Give the position of every malaria parasite.
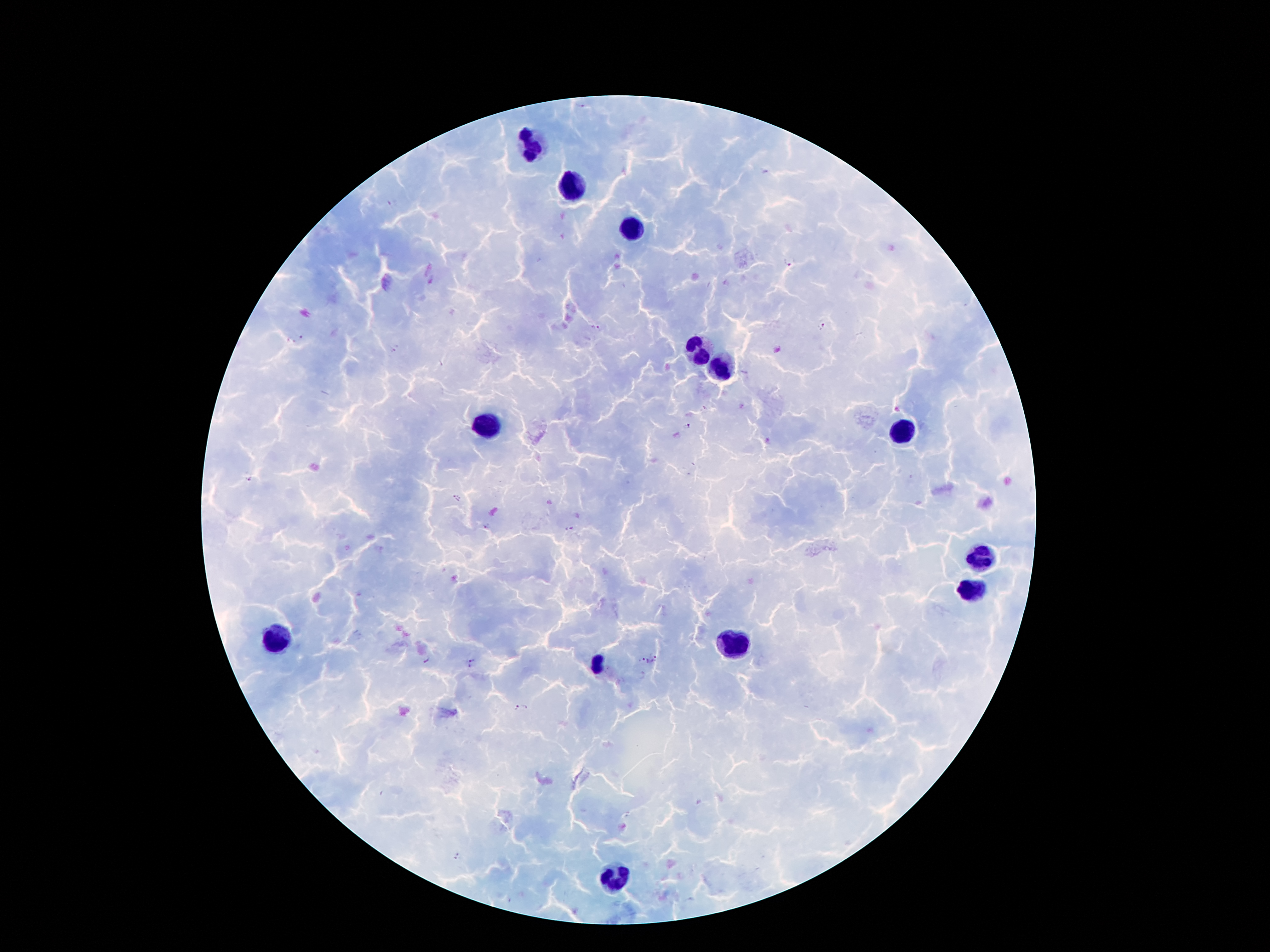

Approximate object centers, in pixels from the top-left corner.
Malaria parasites: (x=392, y=203), (x=790, y=262), (x=823, y=324), (x=598, y=327), (x=303, y=336), (x=291, y=341), (x=396, y=349), (x=688, y=426), (x=248, y=479), (x=457, y=498), (x=486, y=526), (x=569, y=528), (x=427, y=659), (x=656, y=659), (x=471, y=662), (x=646, y=662), (x=516, y=707), (x=525, y=708), (x=457, y=856).

Leukocyte locations: (x=534, y=145), (x=573, y=186), (x=633, y=227), (x=696, y=348), (x=717, y=367), (x=487, y=425), (x=906, y=429), (x=984, y=559), (x=971, y=593), (x=278, y=638), (x=732, y=649), (x=596, y=664), (x=612, y=878). Thick blood smear. Image is 1270×952 pixels. 100x magnification. Patient malaria status: positive for Plasmodium falciparum. One field from this slide. Smartphone photograph taken through the microscope eyepiece. Giemsa-stained preparation.